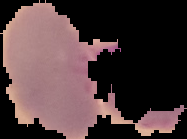

preparation = thin blood smear
image size = 187×139 pixels
malaria status = uninfected
image type = segmented cell region on a black background